Name the parasite shown.
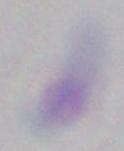
Toxoplasma gondii.

1000x magnification. Photomicrograph.